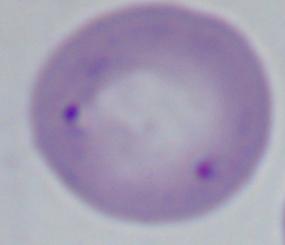

identification = Babesia
modality = photomicrograph
magnification = 1000x